Locate every blood parasite and identify its species.
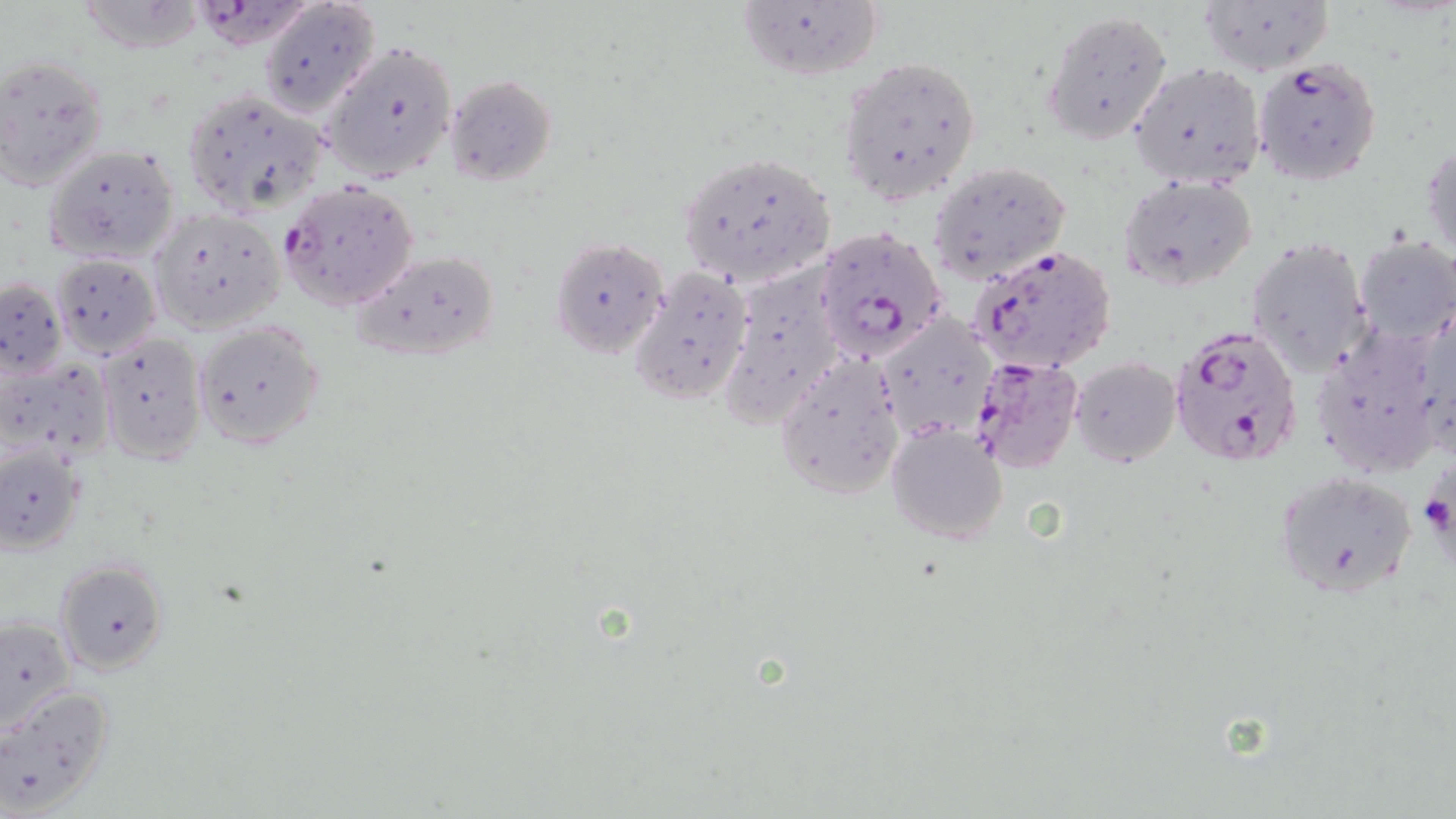
Approximate bounding boxes as (x1,y1)-(x2,y2) corner pairs in pixels.
Plasmodium falciparum-infected red blood cells: (200,0)-(318,58), (1252,56)-(1382,186), (280,180)-(416,309), (815,229)-(945,362), (969,246)-(1119,376), (1168,325)-(1305,471), (970,357)-(1083,473), (1426,470)-(1456,557).
No Plasmodium ovale, Plasmodium malariae, Plasmodium vivax, Babesia divergens, or Trypanosoma brucei observed.

Uninfected red blood cell locations: (75,0)-(205,54), (257,0)-(380,119), (1197,0)-(1333,77), (735,1)-(886,84), (1042,10)-(1171,141), (321,40)-(459,184), (0,53)-(109,189), (839,53)-(982,202), (1127,61)-(1266,190), (444,74)-(557,184), (180,86)-(330,216), (1423,138)-(1455,265), (44,142)-(181,262), (675,153)-(836,285), (929,162)-(1071,281), (1119,176)-(1259,292), (149,206)-(288,333), (1354,236)-(1456,346), (549,238)-(669,358), (1245,238)-(1372,375), (351,250)-(500,362), (51,254)-(161,355), (631,264)-(754,405), (717,267)-(830,441), (0,277)-(66,375), (876,315)-(994,439), (194,320)-(325,450), (1309,320)-(1443,475), (97,333)-(207,462), (775,355)-(907,500), (1070,357)-(1181,467), (886,424)-(1010,547), (0,446)-(84,555), (1272,469)-(1419,599), (55,560)-(168,676), (0,617)-(76,734), (1,687)-(119,815). Slide-level diagnosis: Plasmodium falciparum. Image is 1456×819 pixels. Thin blood smear. Optical microscopy. 1000x magnification. One field of a larger specimen. May-Grünwald-Giemsa-stained preparation.